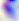 Toxoplasma gondii is seen. Micrograph. 400x magnification.